Classify this cell by malaria status.
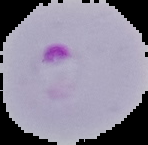

It is parasitized.

From a thin blood film. Image is 148×145 pixels. Segmented cell region on a black background.